Point out each leukocyte.
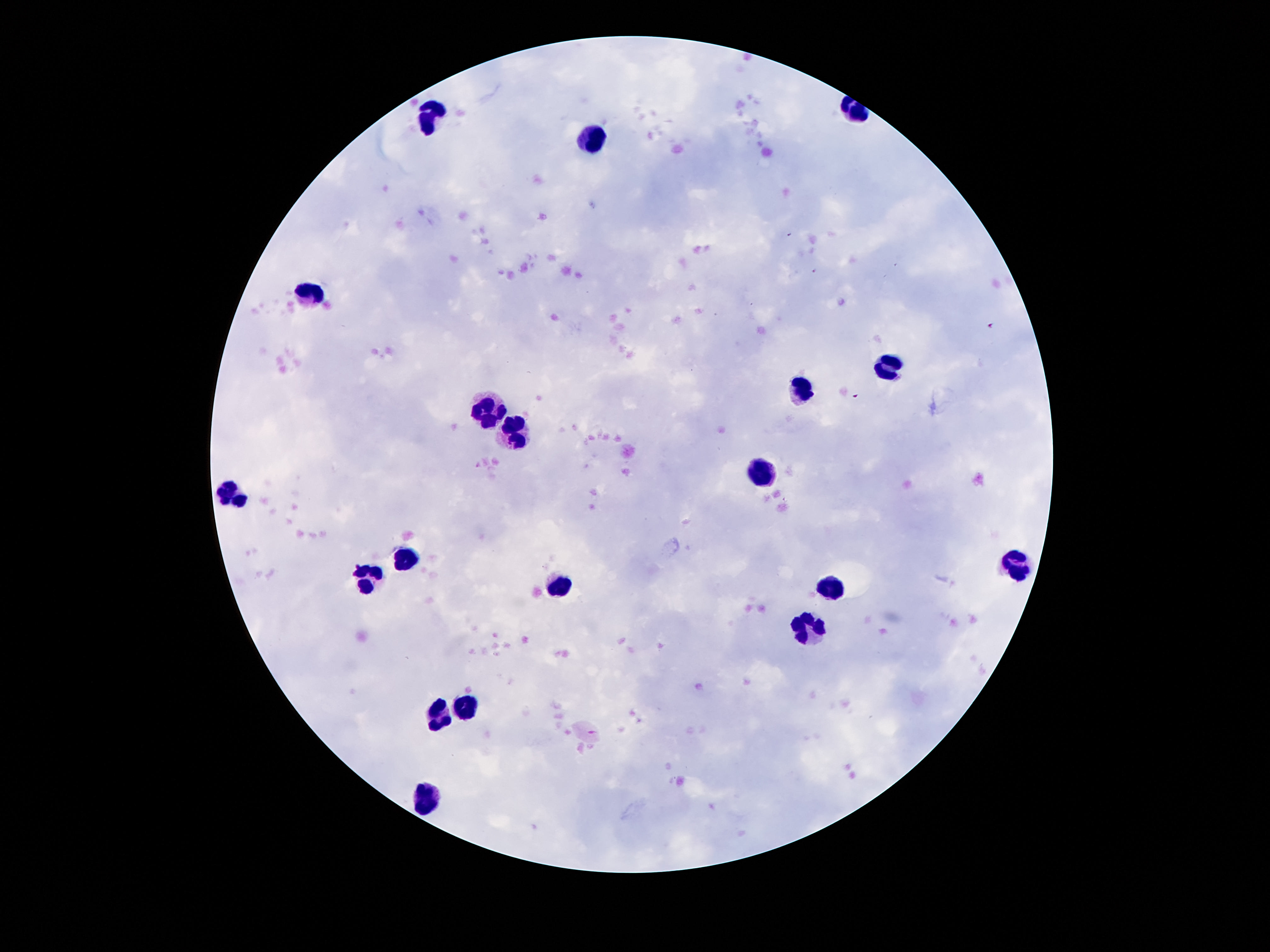
Approximate centers as [x, y] in pixels.
Leukocytes: [431, 116], [599, 136], [309, 290], [886, 368], [802, 392], [484, 407], [513, 436], [763, 471], [234, 492], [409, 558], [1019, 561], [360, 579], [559, 583], [833, 589], [807, 627], [466, 707], [440, 716], [424, 795].

Image is 1270×952 pixels. Smartphone photograph taken through the microscope eyepiece. Thick blood film. Giemsa stain. One field from this slide. Patient malaria status: negative. 100x magnification.